Locate and identify every blood parasite.
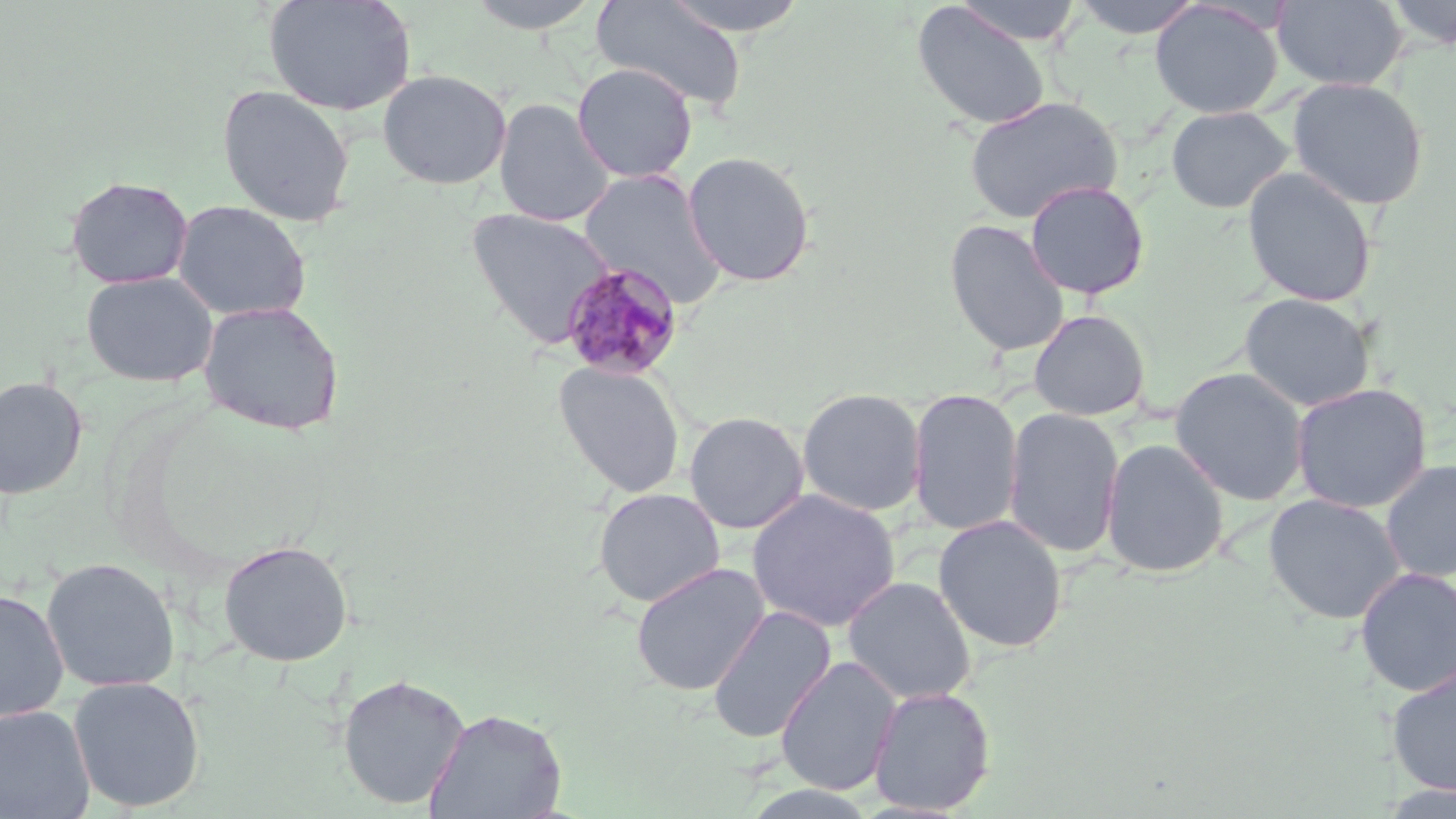

Approximate bounding boxes as (x1, y1, x2, y2) in pixels.
Plasmodium malariae-infected red blood cells: (559, 261, 685, 381).
No Plasmodium falciparum, Plasmodium ovale, Plasmodium vivax, Babesia divergens, or Trypanosoma brucei observed.

Uninfected red blood cell locations: (263, 0, 418, 116), (462, 0, 605, 33), (591, 0, 748, 112), (659, 0, 811, 38), (952, 0, 1086, 46), (1070, 0, 1206, 39), (1272, 0, 1408, 91), (1382, 0, 1456, 49), (1150, 1, 1284, 119), (912, 3, 1051, 131), (571, 62, 698, 183), (377, 69, 512, 190), (1287, 77, 1429, 210), (217, 84, 355, 227), (962, 95, 1123, 225), (494, 97, 615, 227), (1165, 106, 1294, 214), (681, 151, 817, 287), (1241, 167, 1378, 308), (578, 169, 727, 306), (64, 176, 193, 289), (1024, 180, 1150, 299), (171, 199, 312, 321), (465, 206, 615, 349), (943, 218, 1070, 358), (81, 271, 219, 387), (1239, 292, 1376, 412), (198, 300, 345, 436), (1028, 309, 1151, 421), (552, 360, 687, 499), (1169, 367, 1310, 506), (0, 375, 88, 499), (1290, 382, 1433, 513), (797, 388, 927, 516), (906, 388, 1023, 536), (1003, 407, 1125, 559), (683, 410, 810, 534), (1100, 437, 1229, 578), (1380, 458, 1456, 583), (593, 487, 726, 607), (746, 488, 900, 632), (1263, 493, 1406, 625), (932, 515, 1068, 653), (218, 539, 353, 666), (41, 557, 181, 693), (630, 562, 771, 696), (1354, 566, 1456, 698), (842, 575, 977, 705), (0, 588, 69, 723), (707, 605, 837, 744), (775, 655, 902, 796), (1385, 660, 1456, 797), (337, 673, 470, 809), (68, 675, 205, 813), (868, 685, 996, 815), (0, 704, 95, 818), (425, 707, 567, 819), (742, 785, 883, 819). Slide-level diagnosis: Plasmodium malariae. Optical microscopy. Captured at 1000x magnification. May-Grünwald-Giemsa-stained preparation. Image is 1456×819 pixels. Thin blood film. Single field of view.